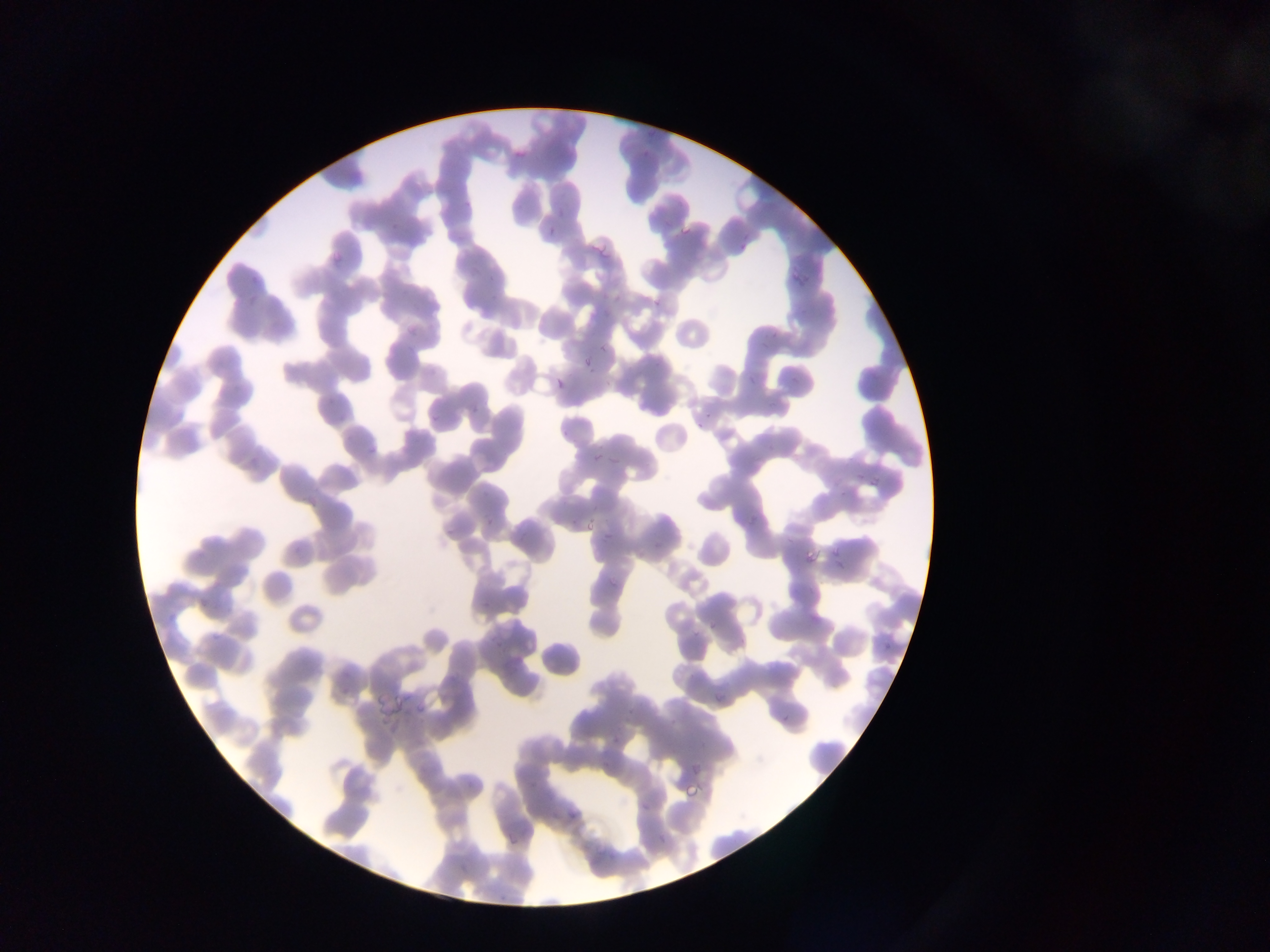

Approximate bounding boxes as left top right bottom in pixels. Malaria parasite locations: 646 125 658 137; 640 147 651 159; 512 148 526 161; 675 219 696 239; 388 222 397 230; 546 226 557 236; 583 230 611 259; 329 248 345 266; 793 262 814 284; 403 318 420 337; 582 356 593 368; 545 375 573 393; 367 442 378 453; 607 455 619 467; 863 468 880 484; 868 473 883 487; 303 494 318 510; 602 531 613 542; 801 549 821 566; 606 575 617 587; 706 617 719 631; 211 628 228 645; 711 690 724 702; 610 735 620 747; 682 779 701 798; 638 801 649 812; 565 807 579 823; 656 835 665 844; 497 894 508 904. Photographed through a microscope with a mobile-phone camera. One field of view. Image is 1270×952 pixels. Sample from Ghana. Thin blood smear.